Point out each malaria parasite.
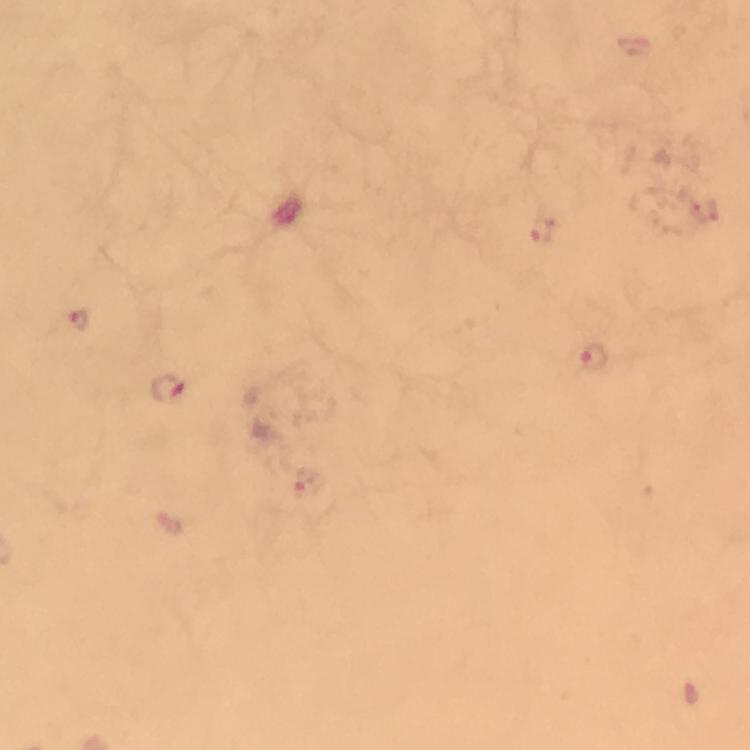
Approximate centers as {x, y} in pixels.
Malaria parasites: {704, 210}, {541, 229}, {79, 323}, {593, 358}, {169, 391}, {309, 485}.

Immersion oil applied. Cropped region of a single field of view. From a diagnostic examination for malaria. Image is 750×750 pixels. Photographed through the microscope with a smartphone camera. Giemsa stain. At 100x magnification. Thick blood smear.